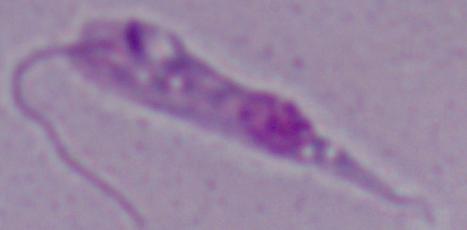
magnification: 1000x
identification: Leishmania
modality: photomicrograph